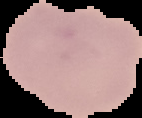
Summary:
  - Image type: segmented cell region on a black background
  - Malaria status: uninfected
  - Preparation: thin blood film
  - Image size: 142×118 pixels